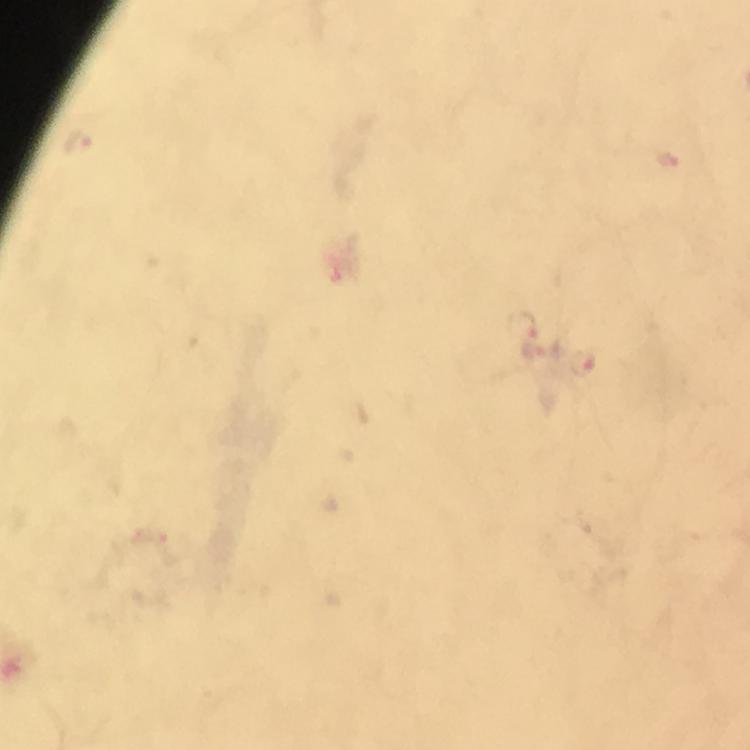

stain = Giemsa
Plasmodium parasite locations = approximate object centers, in pixels from the top-left corner: (x=582, y=363)
capture = smartphone camera through the microscope
preparation = thick smear
immersion oil = used
cropped from = one field of view
context = from a diagnostic examination for malaria
image size = 750×750 pixels
magnification = 100x